Comment on the morphology of the red blood cells.
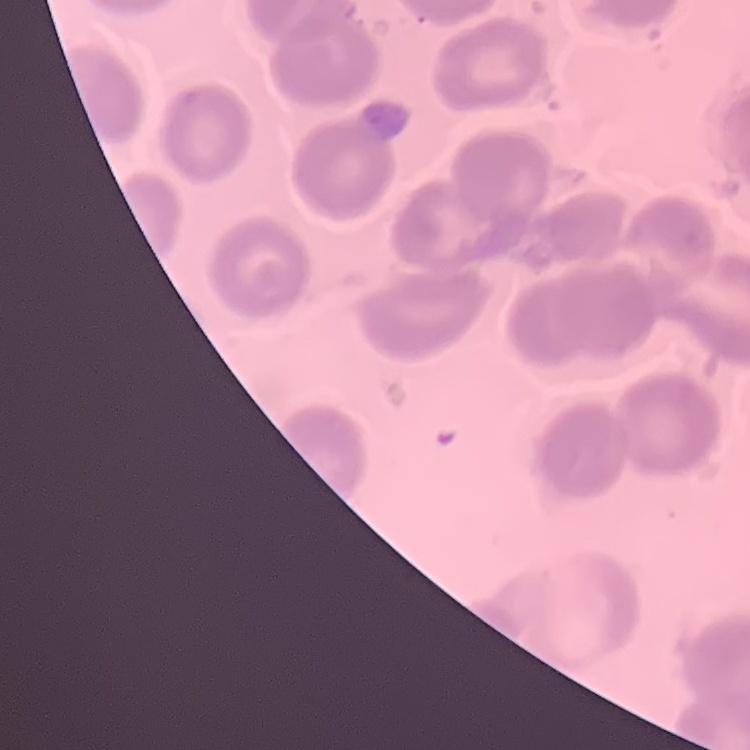
They show no rouleaux formation.

Summary:
  - Preparation: thin blood smear
  - Image type: one tile cut from a larger photomicrograph
  - Stain: Field's or Giemsa